Report the malaria status of this cell.
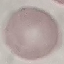
Uninfected.

Giemsa stain. Photographed with a smartphone camera at the microscope eyepiece. Automatically extracted cell patch, resized to 64 × 64 pixels. Thin smear of blood.